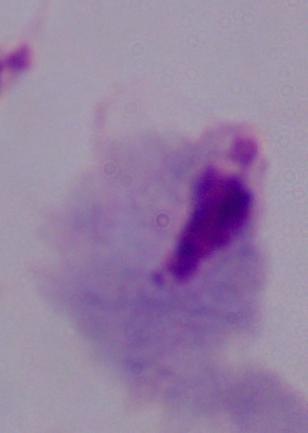
Summary:
  - Magnification: 1000x
  - Identification: trichomonad
  - Modality: micrograph